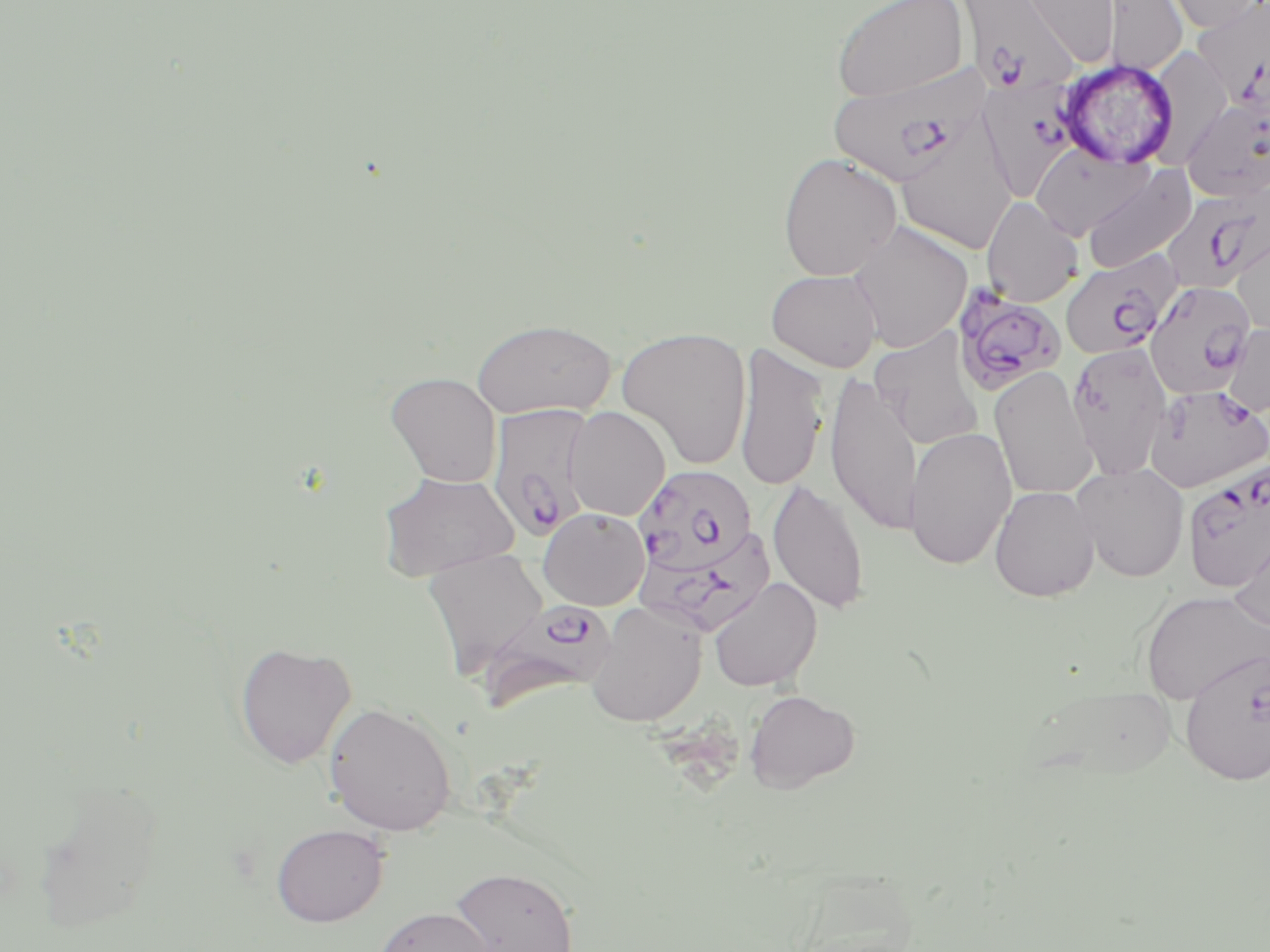

Summary:
  - Coordinate format: approximate bounding boxes as (x1,y1)-(x2,y2) corner pairs in pixels
  - Uninfected red blood cell locations: (831,0)-(970,102), (1017,0)-(1120,67), (1103,0)-(1187,75), (1160,0)-(1267,32), (897,118)-(1018,256), (1031,144)-(1153,241), (777,151)-(903,281), (1081,165)-(1197,273), (981,196)-(1084,307), (848,221)-(972,352), (1232,226)-(1270,339), (766,268)-(883,372), (471,319)-(616,419), (1222,323)-(1270,418), (616,327)-(753,469), (870,327)-(985,450), (1066,341)-(1174,478), (734,344)-(829,491), (990,366)-(1097,500), (386,372)-(502,487), (825,373)-(924,536), (565,407)-(670,521), (903,426)-(1017,570), (1072,461)-(1190,582), (378,471)-(519,581), (768,479)-(871,615), (989,485)-(1099,601), (538,508)-(650,611), (1229,525)-(1269,636), (422,548)-(548,675), (708,577)-(822,692), (1138,589)-(1270,704), (585,601)-(707,727), (234,641)-(356,769), (1178,648)-(1269,785), (744,690)-(860,793), (323,702)-(458,836), (271,823)-(388,926), (447,865)-(579,952), (373,906)-(496,952)
  - Plasmodium falciparum-infected red blood cell locations: (959,0)-(1081,94), (1194,0)-(1270,109), (829,64)-(991,188), (973,79)-(1087,205), (1183,96)-(1269,200), (1160,186)-(1269,293), (1060,252)-(1181,360), (1144,281)-(1256,397), (953,285)-(1067,396), (1144,383)-(1270,493), (487,402)-(597,541), (1183,463)-(1270,593), (633,465)-(758,574), (635,528)-(776,636), (480,598)-(618,710)
  - Slide-level diagnosis: Plasmodium falciparum
  - Field of view: one of a larger specimen
  - Preparation: thin blood film
  - Image size: 1270×952 pixels
  - Stain: May-Grünwald-Giemsa
  - Modality: optical microscopy
  - Magnification: 1000x